Locate every blood parasite and identify its species.
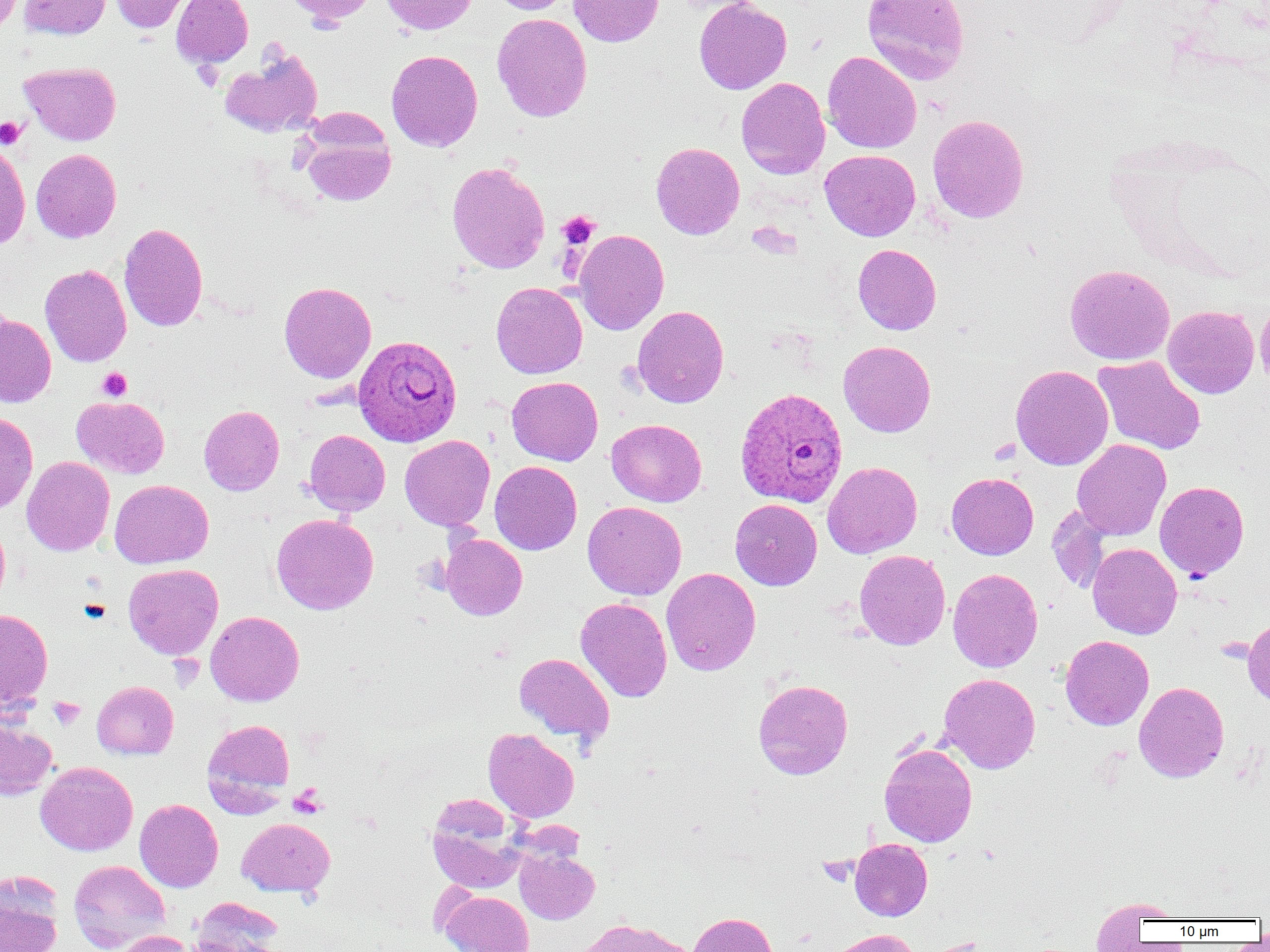

Approximate bounding boxes as (x1, y1, x2, y2) in pixels.
Plasmodium ovale-infected red blood cells: (353, 334, 462, 446), (736, 388, 849, 509).
No Plasmodium falciparum, Plasmodium malariae, Plasmodium vivax, Babesia divergens, or Trypanosoma brucei observed.

{
  "slide_level_diagnosis": "Plasmodium ovale",
  "image_size": "1270×952 pixels",
  "magnification": "1000x",
  "field_of_view": "one of a larger specimen",
  "uninfected_red_blood_cell_locations": "approximate bounding boxes as (x1, y1, x2, y2) in pixels: (0, 0, 23, 34), (19, 0, 110, 40), (110, 0, 195, 33), (171, 0, 253, 68), (281, 0, 380, 24), (381, 0, 477, 35), (490, 0, 575, 14), (568, 0, 664, 47), (694, 0, 792, 94), (862, 0, 970, 84), (492, 13, 593, 122), (219, 48, 323, 138), (386, 49, 483, 152), (822, 51, 922, 154), (20, 62, 121, 145), (736, 77, 830, 179), (927, 114, 1029, 223), (300, 120, 395, 207), (0, 142, 30, 249), (651, 142, 744, 239), (31, 149, 121, 242), (820, 149, 920, 241), (447, 161, 550, 274), (118, 222, 208, 331), (574, 229, 669, 335), (853, 244, 941, 335), (40, 264, 131, 367), (1065, 264, 1174, 365), (279, 281, 376, 383), (491, 282, 587, 378), (1255, 296, 1270, 393), (632, 305, 729, 407), (1163, 305, 1259, 399), (0, 314, 56, 407), (838, 341, 935, 437), (1093, 355, 1206, 455), (1010, 364, 1113, 470), (507, 376, 603, 466), (72, 396, 170, 478), (199, 405, 284, 495), (0, 411, 38, 513), (607, 419, 706, 507), (304, 429, 390, 516), (399, 435, 495, 530), (1072, 439, 1171, 541), (22, 456, 115, 556), (490, 461, 582, 554), (822, 461, 922, 558), (946, 472, 1039, 559), (109, 479, 213, 569), (1155, 480, 1249, 580), (730, 499, 822, 590), (583, 501, 686, 600), (1047, 505, 1111, 594), (271, 513, 378, 615), (0, 518, 10, 611), (441, 533, 527, 620), (1088, 543, 1182, 639), (854, 549, 950, 650), (123, 563, 223, 659), (661, 567, 760, 675), (948, 568, 1043, 672), (576, 598, 672, 702), (0, 609, 53, 711), (205, 611, 304, 706), (1242, 615, 1270, 711), (1060, 635, 1153, 730), (514, 653, 614, 743), (938, 673, 1040, 773), (753, 679, 853, 779), (92, 681, 178, 759), (1134, 681, 1229, 782), (0, 718, 57, 801), (202, 719, 295, 810), (483, 727, 579, 823), (879, 741, 977, 847), (36, 761, 137, 856), (134, 798, 223, 892), (427, 799, 524, 894), (237, 817, 335, 897), (850, 838, 932, 920), (514, 849, 599, 924), (68, 860, 170, 952), (0, 871, 64, 952), (439, 890, 535, 952), (192, 897, 284, 952), (1091, 897, 1185, 928), (688, 912, 777, 952), (573, 919, 696, 952), (825, 928, 923, 952), (109, 931, 197, 952), (919, 937, 998, 952)",
  "preparation": "thin blood film",
  "platelet_locations": "approximate bounding boxes as (x1, y1, x2, y2) in pixels: (0, 118, 26, 148), (557, 211, 600, 248), (98, 367, 132, 401), (48, 697, 86, 729), (289, 784, 327, 817)",
  "modality": "optical microscopy"
}